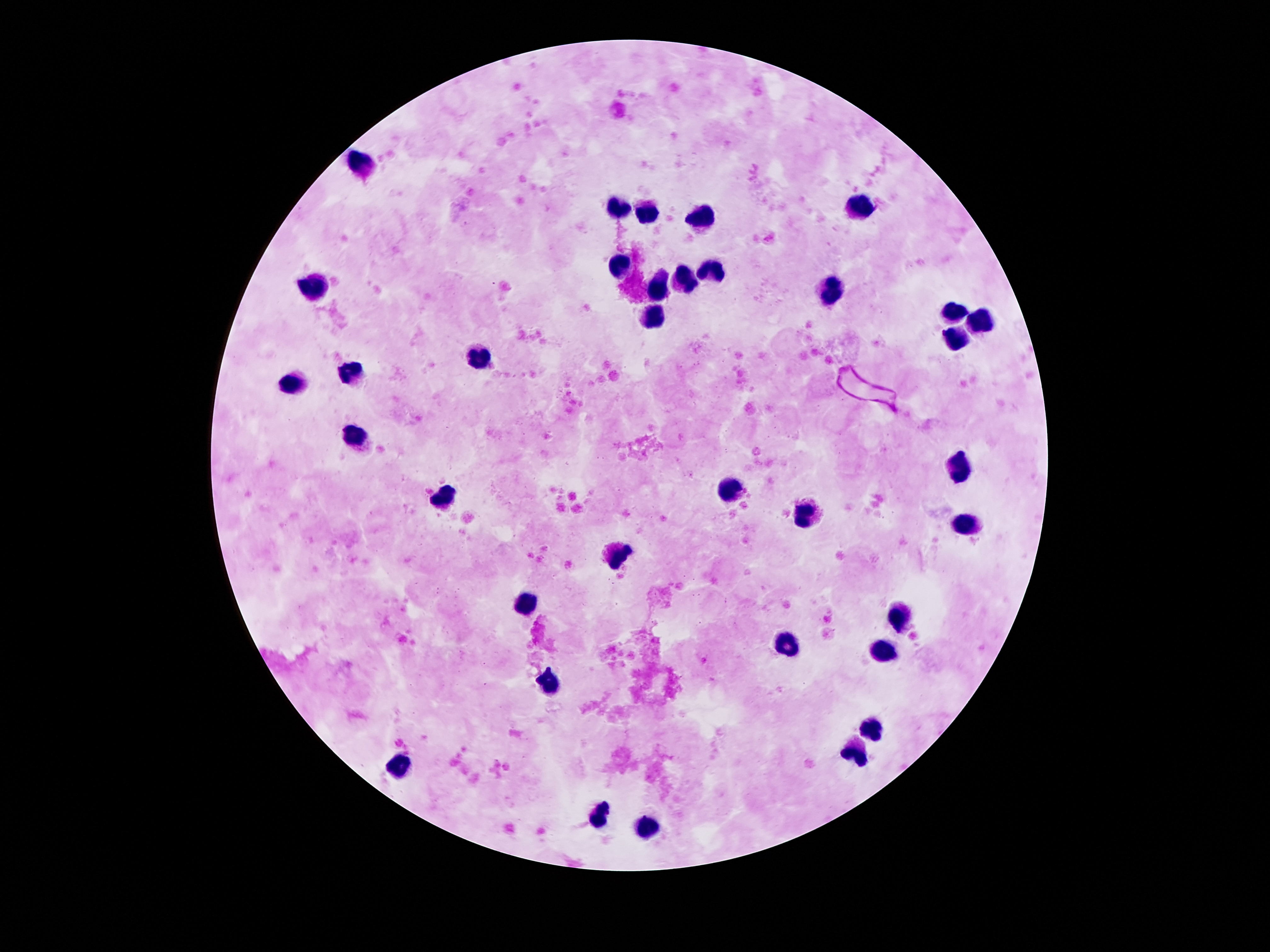

Approximate centers as {x, y} in pixels. Leukocyte locations: {358, 167}, {622, 205}, {860, 209}, {650, 215}, {702, 217}, {618, 269}, {710, 271}, {686, 275}, {315, 283}, {656, 285}, {832, 287}, {956, 309}, {656, 315}, {978, 321}, {954, 335}, {484, 357}, {351, 371}, {297, 379}, {356, 433}, {958, 465}, {728, 489}, {440, 503}, {802, 515}, {966, 525}, {618, 553}, {526, 603}, {894, 617}, {786, 643}, {884, 655}, {548, 681}, {872, 727}, {858, 755}, {398, 763}, {598, 813}, {652, 823}. Thick blood smear. Giemsa stain. 100x magnification. Image is 1270×952 pixels. Single field of view. Smartphone photograph taken through the microscope eyepiece. Patient malaria status: negative.